Name the parasite shown.
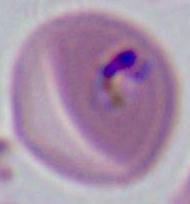
This is Plasmodium.

Summary:
  - Modality: micrograph
  - Magnification: 400x or 1000x